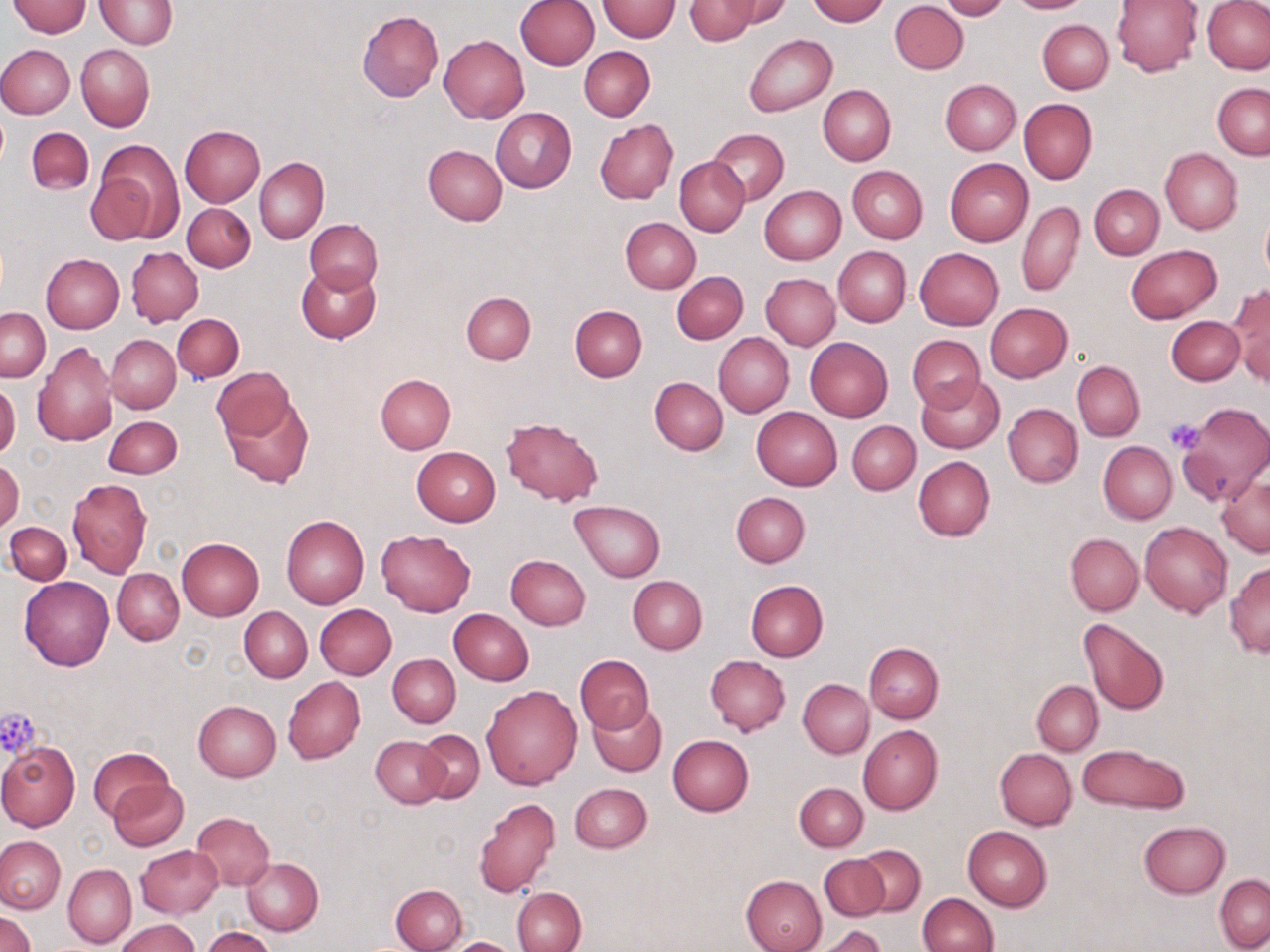

Summary:
  - Coordinate format: approximate bounding boxes as (x1, y1, x2, y2) in pixels
  - Platelet locations: (1163, 418, 1208, 454), (0, 708, 42, 758)
  - Uninfected red blood cell locations: (96, 0, 177, 48), (517, 0, 600, 70), (718, 0, 794, 28), (806, 0, 889, 24), (939, 0, 1009, 21), (1006, 0, 1094, 14), (7, 1, 90, 37), (597, 1, 680, 41), (685, 1, 758, 44), (890, 1, 968, 74), (1111, 1, 1202, 76), (1202, 2, 1270, 74), (357, 11, 444, 102), (1037, 19, 1113, 94), (743, 33, 836, 116), (438, 35, 529, 124), (0, 44, 74, 119), (76, 44, 155, 132), (579, 47, 654, 121), (940, 79, 1020, 155), (1212, 83, 1270, 159), (818, 84, 895, 165), (1019, 98, 1097, 184), (490, 107, 577, 193), (595, 119, 677, 204), (179, 125, 266, 207), (27, 127, 94, 195), (709, 129, 788, 202), (91, 141, 183, 245), (422, 145, 507, 225), (1160, 148, 1242, 235), (255, 157, 328, 244), (675, 157, 749, 236), (945, 158, 1033, 246), (847, 166, 927, 243), (1089, 184, 1164, 259), (760, 186, 846, 265), (1018, 200, 1085, 297), (183, 202, 255, 272), (1260, 207, 1270, 285), (620, 218, 700, 294), (305, 219, 383, 293), (1125, 245, 1221, 323), (833, 246, 911, 326), (127, 247, 203, 326), (914, 248, 1003, 331), (42, 253, 124, 333), (294, 263, 380, 344), (671, 272, 748, 344), (761, 273, 840, 350), (1228, 284, 1270, 384), (461, 292, 536, 365), (985, 303, 1071, 382), (570, 305, 646, 381), (1, 308, 50, 381), (172, 314, 243, 382), (1166, 316, 1245, 385), (713, 332, 794, 417), (908, 334, 986, 411), (106, 335, 180, 413), (804, 337, 892, 422), (32, 342, 117, 446), (1073, 360, 1144, 441), (213, 368, 296, 441), (376, 374, 456, 454), (916, 375, 1005, 455), (649, 376, 728, 454), (0, 381, 20, 459), (220, 386, 313, 488), (1178, 402, 1269, 503), (1003, 403, 1082, 489), (751, 406, 841, 491), (104, 416, 182, 478), (496, 418, 603, 509), (848, 420, 921, 495), (1098, 440, 1178, 524), (411, 447, 501, 526), (913, 456, 995, 541), (1, 458, 23, 534), (1217, 475, 1270, 556), (68, 478, 152, 577), (731, 491, 810, 567), (570, 500, 666, 580), (281, 515, 369, 608), (1140, 521, 1232, 617), (4, 522, 71, 585), (376, 529, 476, 615), (1065, 533, 1143, 616), (176, 538, 264, 621), (505, 554, 591, 630), (1225, 563, 1270, 655), (113, 568, 183, 645), (627, 576, 707, 653), (20, 577, 114, 670), (746, 581, 828, 662), (314, 603, 396, 679), (240, 607, 312, 682), (448, 608, 534, 685), (1078, 618, 1169, 715), (864, 641, 944, 723), (388, 654, 460, 727), (575, 655, 654, 735), (705, 655, 790, 735), (283, 676, 365, 763), (798, 679, 873, 758), (1032, 680, 1103, 755), (481, 684, 584, 790), (589, 699, 667, 777), (193, 700, 282, 782), (859, 724, 942, 814), (415, 729, 484, 803), (667, 734, 754, 816), (372, 736, 447, 808), (0, 742, 79, 832), (1076, 743, 1189, 815), (88, 746, 173, 821), (995, 748, 1077, 829), (107, 779, 188, 850), (569, 782, 652, 853), (794, 782, 868, 851), (474, 797, 560, 898), (190, 812, 275, 891), (1139, 820, 1230, 899), (962, 825, 1052, 911), (0, 836, 65, 913), (135, 845, 222, 918), (855, 846, 925, 916), (819, 854, 889, 921), (241, 857, 323, 936), (63, 864, 137, 948), (740, 874, 827, 952), (1215, 874, 1270, 951), (391, 883, 467, 952), (513, 887, 587, 952), (917, 893, 998, 952), (0, 912, 35, 952), (116, 918, 201, 952), (809, 926, 887, 952), (203, 928, 276, 952), (443, 936, 524, 952)
  - Slide-level diagnosis: no evidence of blood parasites
  - Image size: 1270×952 pixels
  - Stain: May-Grünwald-Giemsa
  - Magnification: 1000x
  - Preparation: thin blood film
  - Modality: light microscopy
  - Field of view: single